Identify the blood parasite species.
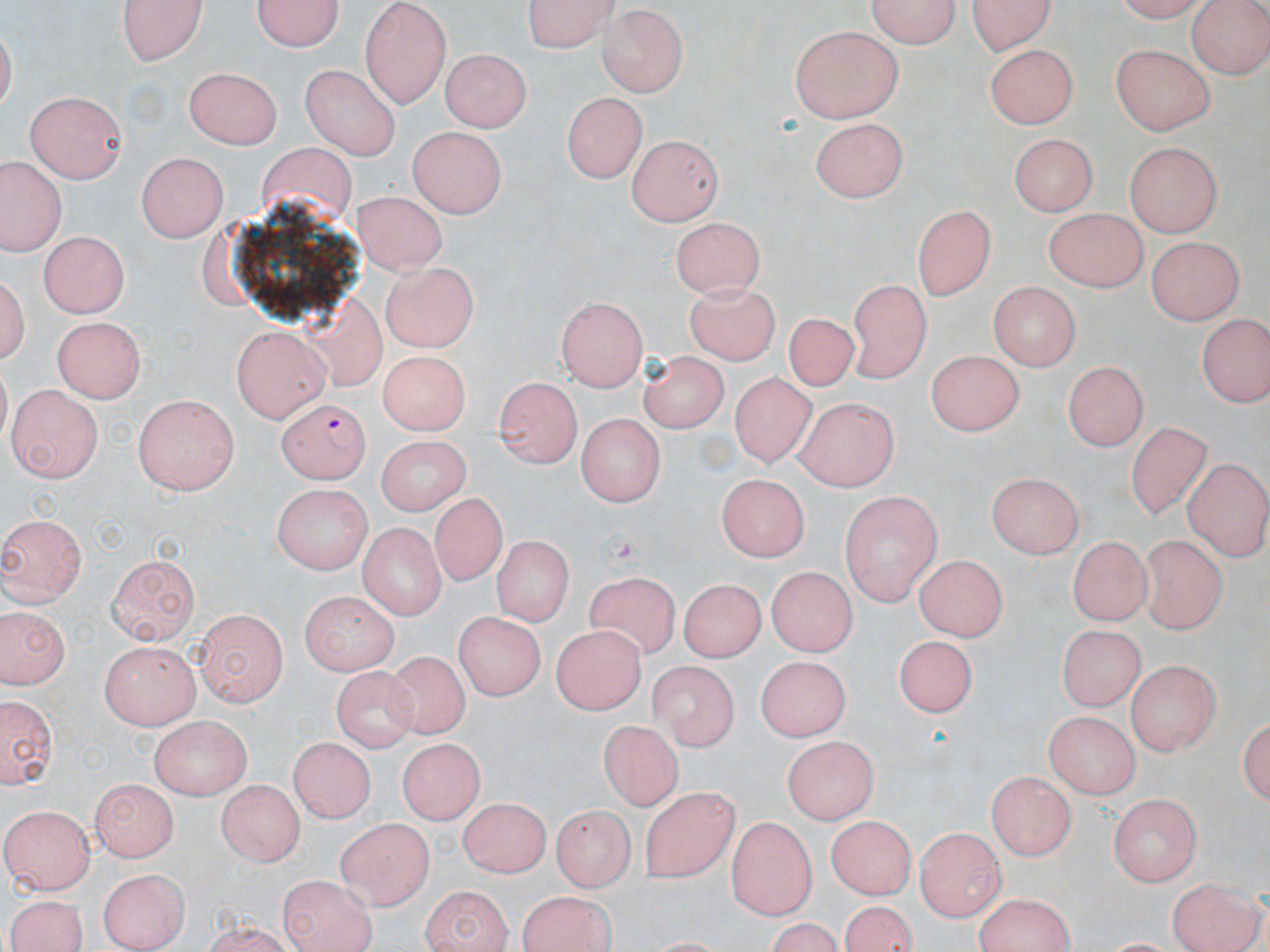
Plasmodium falciparum.

field of view = single
Plasmodium falciparum-infected red blood cell locations = approximate bounding boxes as (x1, y1, x2, y2) in pixels: (278, 397, 370, 481)
image size = 1270×952 pixels
modality = light microscopy
preparation = thin blood film
uninfected red blood cell locations = approximate bounding boxes as (x1, y1, x2, y2) in pixels: (118, 0, 210, 64), (252, 0, 347, 54), (359, 0, 452, 102), (525, 0, 622, 53), (864, 0, 961, 52), (966, 0, 1059, 55), (1113, 0, 1212, 23), (1185, 0, 1269, 80), (595, 7, 686, 95), (789, 26, 904, 122), (984, 42, 1080, 129), (1111, 42, 1216, 135), (442, 46, 529, 131), (301, 64, 404, 156), (186, 65, 280, 147), (562, 90, 647, 183), (25, 93, 128, 184), (812, 117, 906, 201), (410, 128, 504, 217), (1006, 133, 1100, 215), (626, 134, 721, 224), (1123, 142, 1226, 237), (253, 148, 361, 202), (138, 151, 228, 240), (0, 157, 66, 255), (350, 190, 447, 270), (912, 201, 997, 300), (1041, 208, 1149, 292), (671, 214, 767, 299), (39, 230, 131, 317), (1146, 234, 1247, 323), (380, 260, 480, 352), (3, 266, 33, 372), (845, 276, 931, 381), (990, 279, 1081, 373), (682, 284, 780, 365), (374, 291, 480, 427), (554, 295, 650, 391), (785, 314, 860, 397), (1199, 314, 1268, 410), (306, 316, 390, 391), (51, 318, 146, 403), (231, 322, 331, 421), (926, 348, 1020, 437), (380, 351, 469, 435), (635, 351, 726, 429), (1063, 358, 1151, 450), (729, 375, 813, 467), (495, 376, 582, 469), (7, 383, 102, 479), (132, 393, 240, 492), (793, 398, 901, 488), (576, 413, 666, 503), (1124, 418, 1212, 522), (374, 433, 474, 515), (1184, 459, 1270, 558), (717, 470, 813, 553), (988, 471, 1087, 554), (267, 483, 373, 572), (838, 492, 942, 605), (427, 495, 509, 581), (0, 514, 86, 608), (355, 521, 446, 619), (1139, 531, 1224, 637), (493, 535, 574, 629), (1070, 536, 1147, 625), (105, 552, 200, 645), (915, 552, 1005, 642), (768, 569, 855, 654), (584, 571, 685, 660), (675, 578, 771, 659), (298, 588, 402, 677), (0, 607, 69, 691), (451, 608, 543, 703), (192, 610, 290, 707), (549, 623, 645, 714), (1054, 623, 1149, 708), (894, 634, 978, 715), (96, 641, 203, 728), (378, 652, 474, 740), (754, 655, 852, 739), (646, 658, 738, 751), (1127, 660, 1221, 754), (333, 667, 417, 757), (2, 693, 57, 792), (1044, 709, 1137, 800), (1240, 709, 1270, 813), (150, 717, 249, 801), (600, 724, 678, 811), (779, 736, 880, 822), (396, 739, 483, 825), (290, 740, 375, 823), (987, 770, 1078, 859), (91, 776, 177, 858), (218, 778, 305, 868), (638, 784, 738, 880), (459, 796, 550, 879), (1108, 796, 1200, 886), (549, 803, 635, 891), (4, 804, 95, 893), (826, 815, 915, 899), (338, 816, 436, 909), (726, 816, 816, 921), (913, 827, 1004, 920), (98, 866, 189, 952), (279, 873, 377, 952), (1168, 875, 1265, 952), (419, 884, 511, 952), (516, 890, 618, 952), (970, 892, 1073, 952), (2, 894, 92, 952), (838, 899, 919, 952)
magnification = 1000x
stain = May-Grünwald-Giemsa